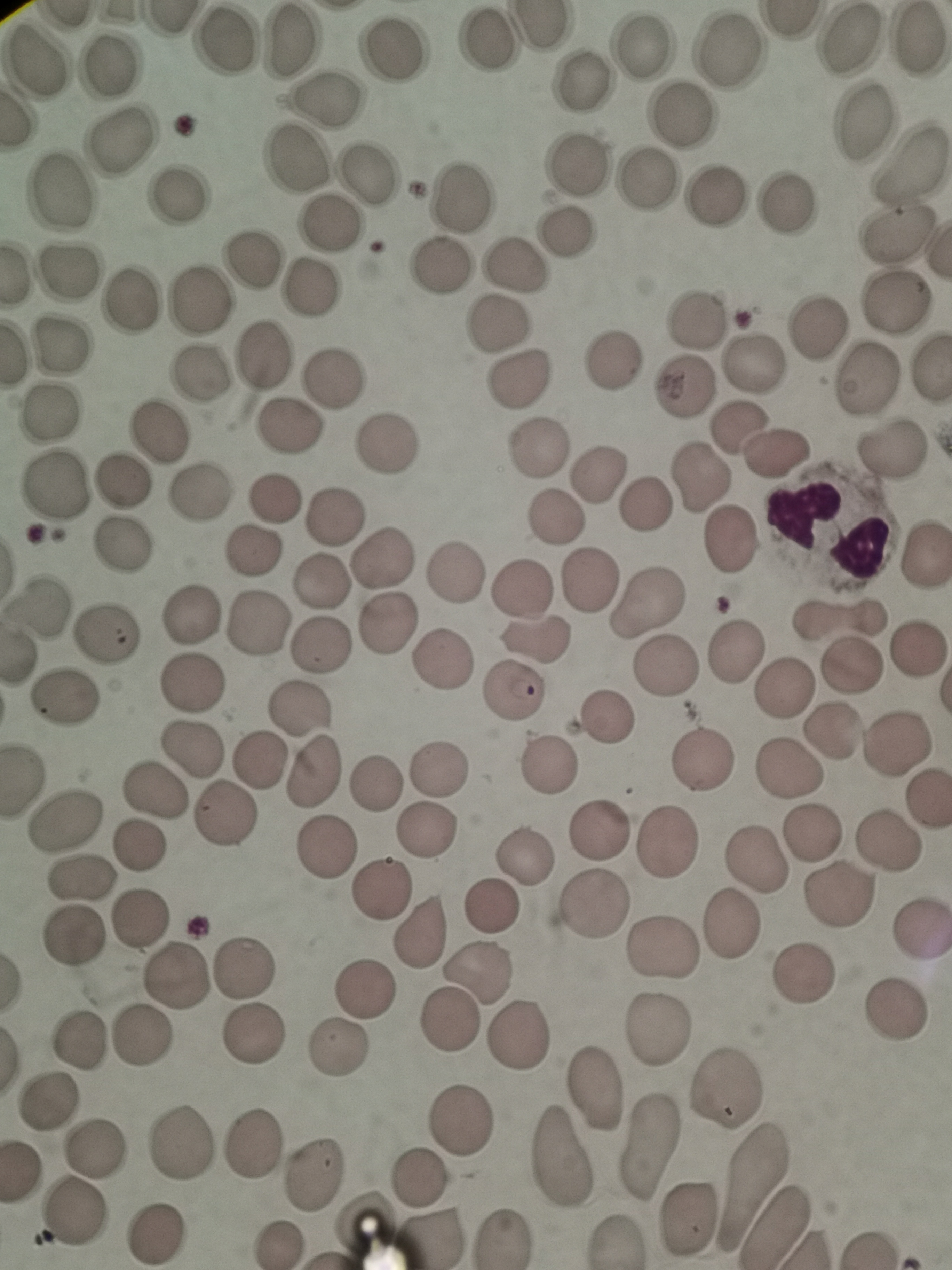
Approximate centers as [x, y] in pixels. Cell locations: [849, 40], [918, 40], [289, 43], [486, 44], [225, 45], [641, 46], [396, 51], [730, 51], [38, 62], [110, 67], [580, 83], [327, 99], [681, 115], [861, 120], [118, 139], [298, 159], [576, 165], [911, 166], [373, 173], [647, 178], [61, 190], [463, 191], [182, 195], [712, 198], [786, 202], [329, 223], [564, 232], [893, 233], [255, 260], [512, 263], [438, 265], [69, 272], [313, 288], [131, 299], [894, 300], [201, 301], [695, 319], [497, 322], [818, 332], [67, 345], [263, 356], [611, 358], [753, 363], [201, 372], [868, 377], [335, 378], [519, 381], [683, 388], [49, 412], [288, 425], [741, 427], [157, 430], [387, 441], [891, 449], [538, 450], [774, 450], [598, 474], [697, 476], [121, 480], [58, 486], [202, 491], [276, 497], [648, 506], [337, 517], [554, 518], [733, 538], [124, 543], [251, 552], [922, 553], [382, 555], [456, 574], [591, 581], [318, 583], [521, 588], [41, 601], [651, 604], [189, 613], [838, 620], [256, 622], [389, 622], [109, 633], [536, 637], [320, 648], [733, 651], [916, 651], [441, 660], [667, 664], [852, 666], [189, 683], [781, 684], [511, 692], [65, 697], [304, 710], [606, 716], [837, 733], [899, 741], [196, 747], [259, 760], [706, 762], [547, 767], [438, 768], [790, 770], [310, 773], [374, 785], [152, 792], [220, 813], [71, 815], [426, 829], [600, 829], [812, 831], [668, 842], [888, 842], [140, 847], [325, 849], [525, 857], [758, 859], [81, 879], [379, 891], [841, 897], [490, 906], [594, 906], [141, 914], [731, 928], [919, 930], [418, 933], [75, 940], [663, 950], [245, 963], [482, 971], [799, 973], [177, 978], [362, 992], [896, 1009], [449, 1020], [656, 1028], [521, 1034], [142, 1036], [81, 1039], [254, 1041], [338, 1051], [593, 1086], [728, 1087], [55, 1104], [462, 1120], [180, 1138], [254, 1143], [651, 1143], [95, 1146], [566, 1157], [316, 1172], [419, 1180], [754, 1183], [686, 1213], [76, 1214], [154, 1233], [505, 1238], [434, 1239]. Single field of view. Image is 952×1270 pixels. Photographed with a smartphone camera at the microscope eyepiece. Giemsa-stained preparation. Thin smear of blood.